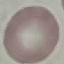

Summary:
  - Result: no malaria parasites detected
  - Image type: automatically extracted cell patch, resized to 64 × 64 pixels
  - Capture: smartphone through the microscope eyepiece
  - Preparation: thin smear
  - Stain: Giemsa